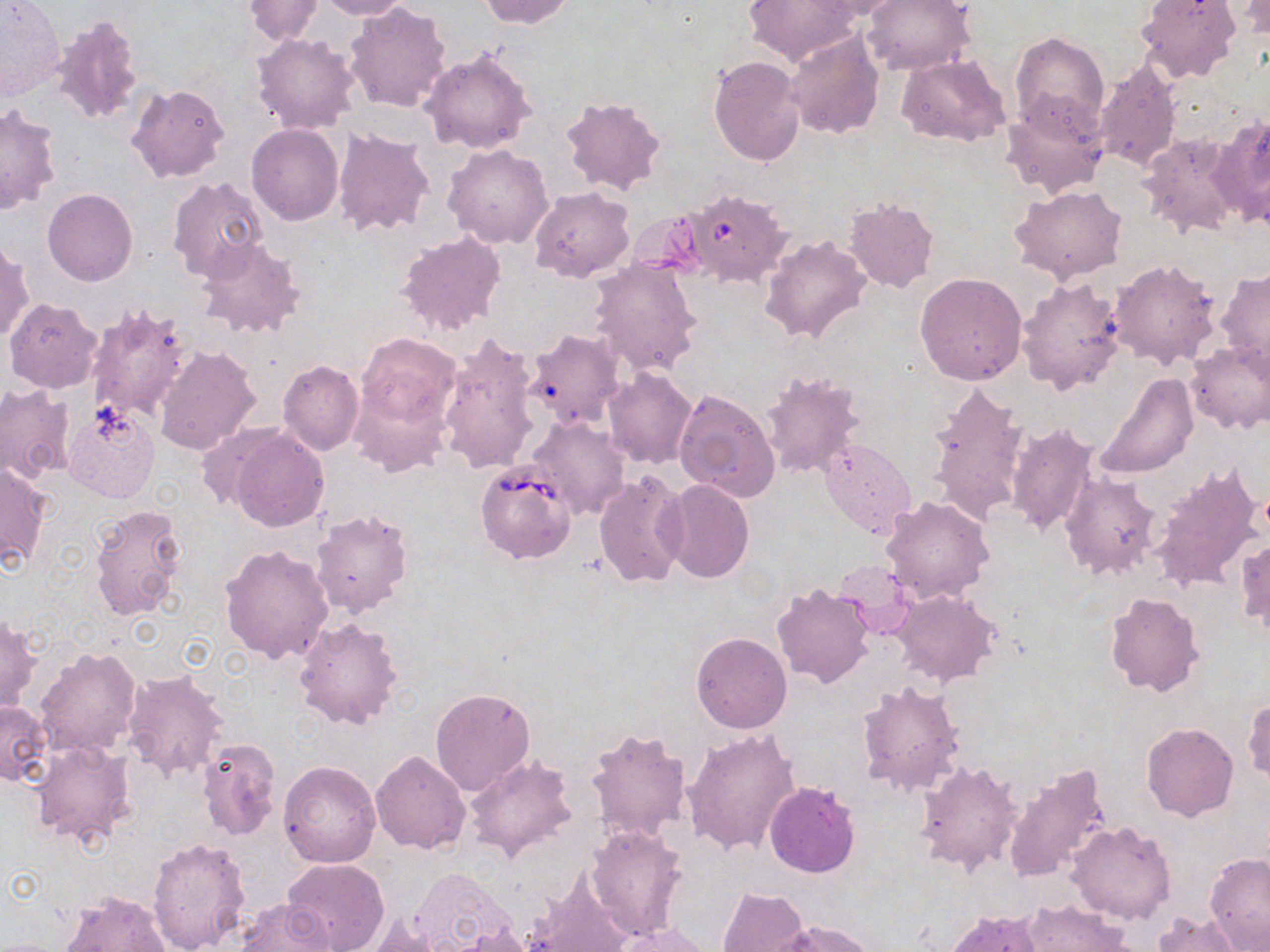 Approximate bounding boxes as [x1, y1, x2, y2] in pixels. Babesia divergens-infected red blood cell locations: [680, 194, 798, 291], [475, 461, 578, 564]. Uninfected red blood cell locations: [243, 0, 325, 45], [308, 0, 411, 19], [478, 0, 575, 28], [742, 0, 859, 67], [809, 0, 917, 20], [863, 0, 975, 76], [1135, 0, 1240, 85], [1233, 0, 1270, 42], [0, 2, 65, 101], [344, 2, 452, 112], [50, 15, 146, 126], [783, 31, 884, 140], [250, 32, 362, 135], [1010, 33, 1108, 130], [1041, 38, 1150, 154], [420, 49, 537, 154], [898, 54, 1012, 148], [709, 55, 805, 165], [1093, 58, 1180, 173], [126, 83, 232, 183], [1000, 92, 1109, 198], [559, 95, 668, 197], [0, 105, 62, 216], [1212, 112, 1270, 227], [246, 124, 343, 226], [333, 128, 436, 238], [1137, 131, 1244, 238], [443, 144, 555, 249], [166, 177, 269, 284], [1009, 184, 1128, 284], [528, 186, 634, 282], [43, 188, 137, 286], [843, 198, 940, 294], [625, 209, 710, 284], [395, 231, 508, 336], [759, 235, 872, 345], [194, 237, 306, 341], [0, 240, 33, 345], [587, 259, 704, 376], [1108, 259, 1221, 370], [1216, 267, 1270, 371], [915, 271, 1027, 385], [1017, 276, 1127, 396], [4, 298, 102, 393], [84, 303, 192, 427], [523, 328, 627, 430], [435, 333, 540, 476], [355, 334, 462, 429], [1186, 339, 1270, 435], [153, 345, 260, 457], [277, 361, 364, 456], [604, 369, 699, 468], [760, 370, 866, 479], [1093, 372, 1199, 480], [925, 382, 1030, 526], [0, 383, 75, 484], [351, 385, 449, 477], [671, 386, 780, 502], [63, 403, 161, 503], [529, 416, 629, 518], [1005, 423, 1100, 538], [225, 426, 331, 533], [819, 437, 915, 540], [1, 462, 52, 572], [1149, 462, 1265, 594], [594, 468, 690, 589], [1059, 470, 1161, 580], [661, 479, 754, 583], [880, 495, 996, 604], [87, 502, 189, 622], [310, 509, 413, 618], [1236, 535, 1269, 639], [219, 545, 334, 665], [833, 561, 917, 640], [770, 584, 876, 689], [893, 590, 1001, 687], [1103, 591, 1205, 698], [0, 612, 40, 714], [293, 618, 404, 731], [690, 631, 792, 734], [35, 646, 142, 757], [121, 669, 229, 781], [856, 679, 967, 799], [430, 687, 535, 795], [1243, 696, 1270, 785], [0, 700, 52, 786], [1141, 723, 1239, 822], [584, 725, 694, 844], [682, 730, 798, 857], [195, 738, 281, 842], [27, 739, 136, 852], [370, 750, 470, 854], [464, 753, 576, 862], [915, 759, 1023, 875], [278, 761, 381, 868], [1003, 764, 1113, 883], [765, 782, 861, 878], [1066, 820, 1176, 923], [584, 824, 689, 940], [146, 837, 251, 951], [1204, 852, 1270, 949], [283, 858, 390, 952], [408, 869, 510, 949], [526, 869, 632, 952], [719, 886, 809, 951], [60, 891, 171, 951], [235, 899, 340, 952], [1021, 901, 1135, 950], [942, 909, 1044, 952], [1152, 912, 1242, 952], [777, 919, 874, 952], [612, 922, 714, 951], [450, 925, 537, 952]. Slide-level diagnosis: Babesia divergens. 1000x magnification. One field of a larger specimen. Thin blood film. Image is 1270×952 pixels. Optical microscopy. May-Grünwald-Giemsa-stained preparation.